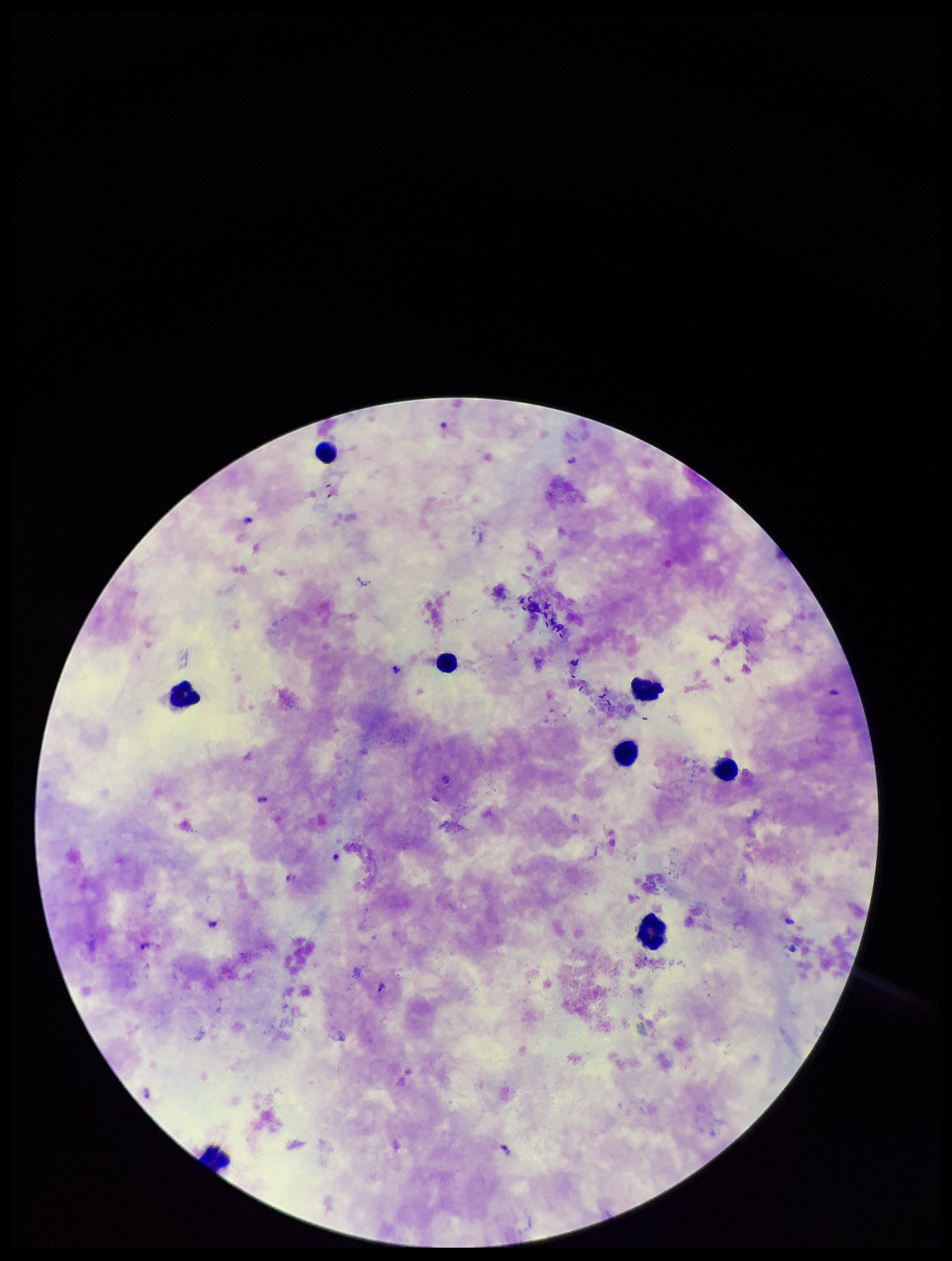
image_size: 952×1261 pixels
field_of_view: one from this slide
patient_malaria_status: positive
capture: smartphone photograph through the microscope eyepiece
leukocyte_count: 8
preparation: thick smear
stain: Giemsa
plasmodium_parasites: identified
species_reported_for_this_patient: Plasmodium falciparum
parasite_count: 6